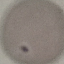

Summary:
  - Result: no malaria parasites seen
  - Image type: automatically extracted cell patch, resized to 64 × 64 pixels
  - Stain: Giemsa
  - Preparation: thin blood smear
  - Capture: smartphone camera at the microscope eyepiece